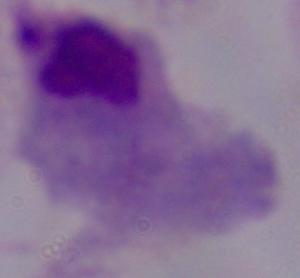
Summary:
  - Identification: trichomonad
  - Modality: photomicrograph
  - Magnification: 1000x